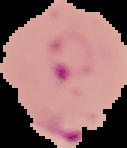

preparation = thin blood smear
image size = 127×148 pixels
image type = segmented cell region on a black background
result = Plasmodium parasites detected